Give the position of every malaria parasite.
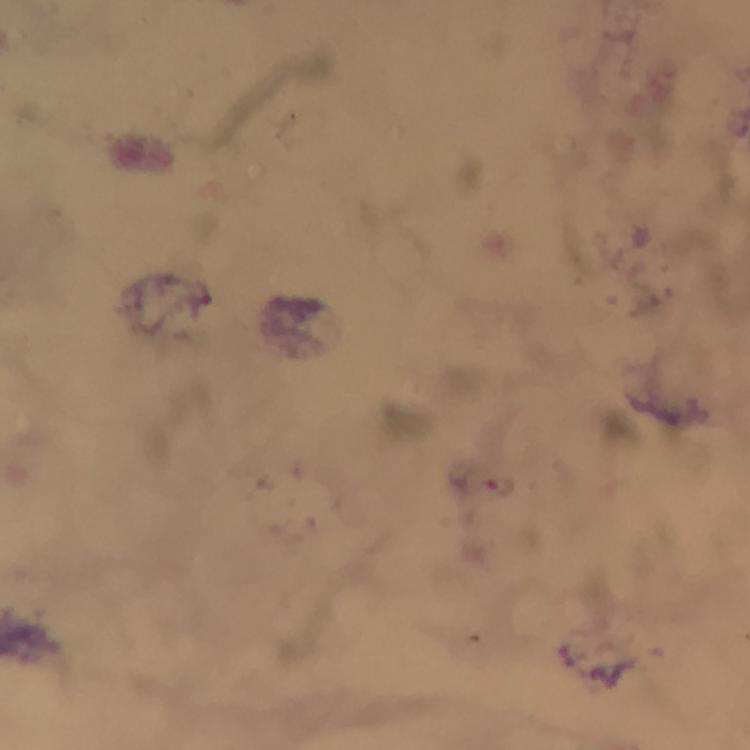
Approximate centers as (x, y) in pixels.
Malaria parasites: (500, 488).

From a malaria diagnostic workup. Image is 750×750 pixels. At 100x magnification. Giemsa stain. Thick smear. Immersion oil was used. A crop from one field of view. Photographed with a smartphone mounted on the microscope.